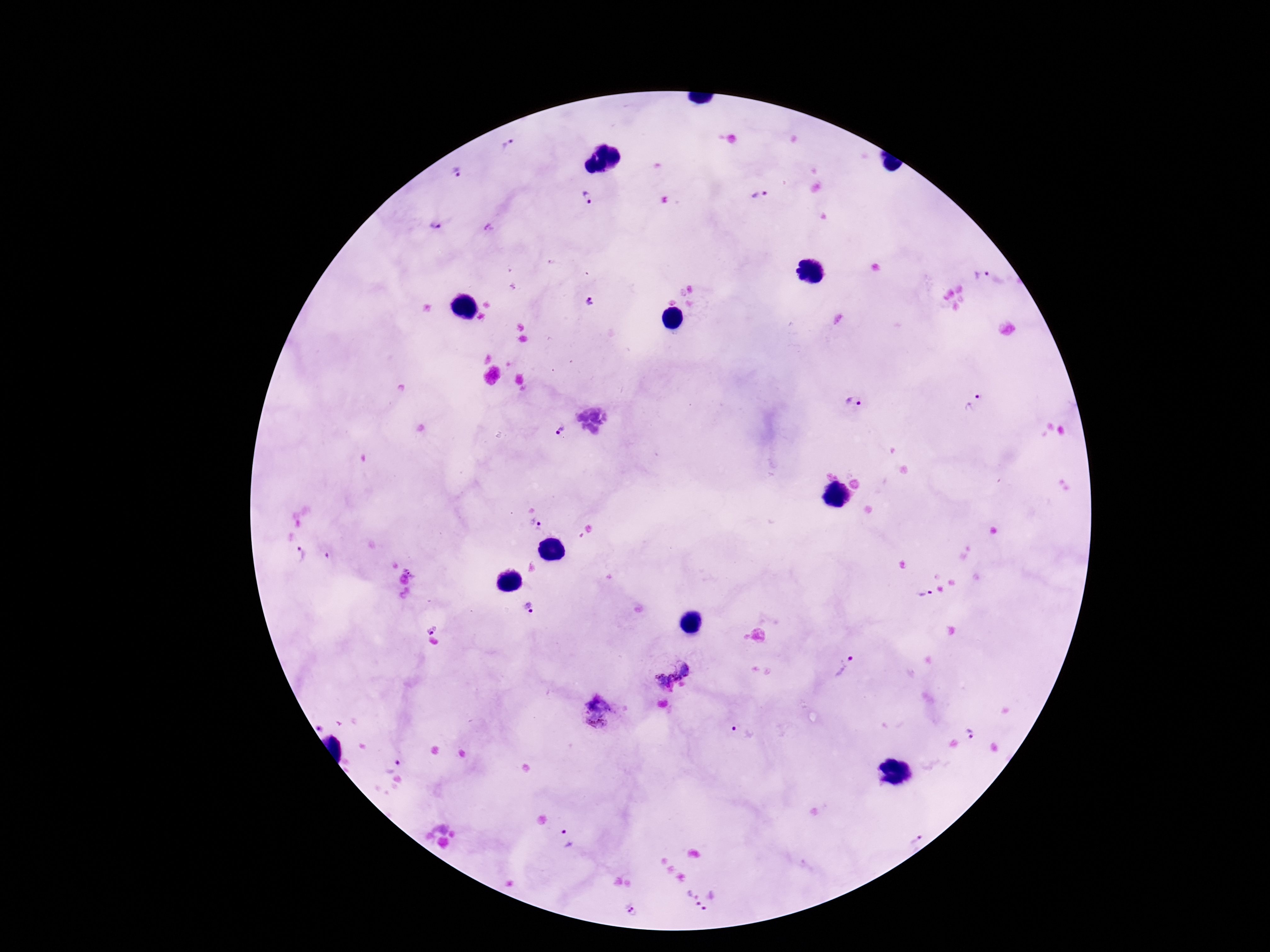
Approximate object centers, in pixels from the top-left corner.
Summary:
  - Plasmodium parasite locations: (x=507, y=148), (x=458, y=173), (x=760, y=195), (x=586, y=196), (x=435, y=225), (x=981, y=273), (x=589, y=301), (x=854, y=401), (x=972, y=402), (x=560, y=430), (x=536, y=524), (x=299, y=554), (x=925, y=594), (x=529, y=608), (x=432, y=626), (x=672, y=668), (x=843, y=669), (x=599, y=714), (x=741, y=733), (x=969, y=734), (x=392, y=764), (x=913, y=836), (x=568, y=840), (x=693, y=897), (x=716, y=905), (x=630, y=910)
  - Preparation: thick peripheral-blood smear
  - Image size: 1270×952 pixels
  - Patient malaria status: infected
  - Magnification: 100x
  - Capture: smartphone camera through the microscope eyepiece
  - Field of view: one from this slide
  - Stain: Giemsa